Assess the morphology of the red blood cells.
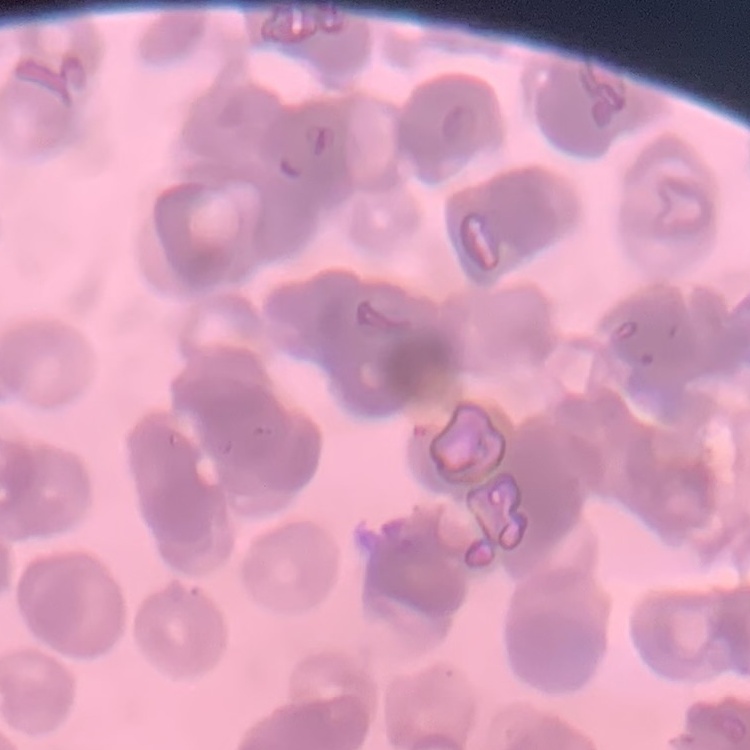

They show rouleaux formation.

Summary:
  - Image type: one tile cut from a larger photomicrograph
  - Stain: Field's or Giemsa
  - Preparation: thin peripheral smear